Name the blood parasite species.
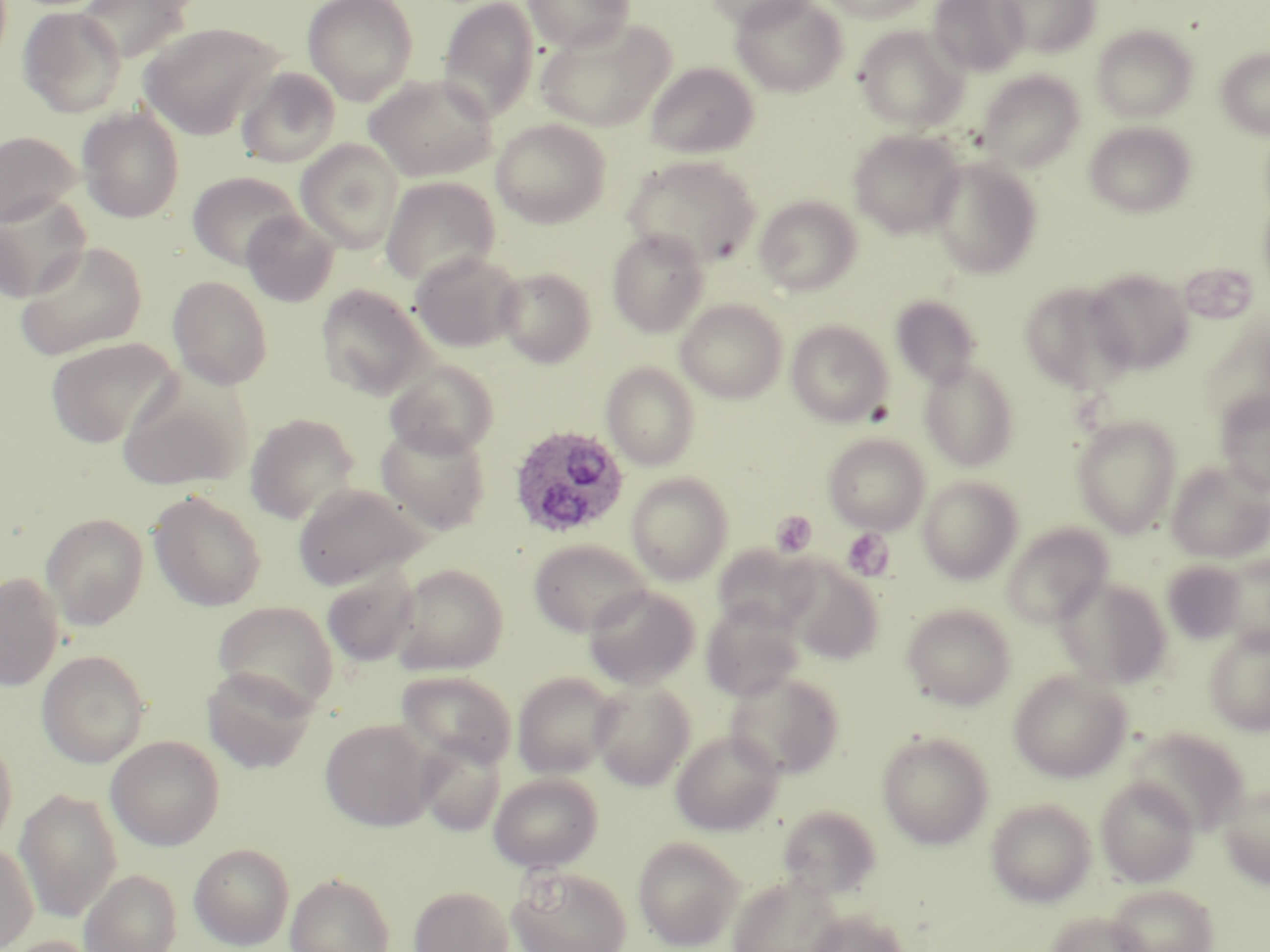

Plasmodium ovale.

magnification = 1000x
Plasmodium ovale-infected red blood cell locations = approximate bounding boxes as [x1, y1, x2, y2] in pixels: [508, 424, 629, 539]
field of view = one of a larger specimen
modality = light microscopy
image size = 1270×952 pixels
stain = May-Grünwald-Giemsa
uninfected red blood cell locations = approximate bounding boxes as [x1, y1, x2, y2] in pixels: [302, 0, 418, 104], [524, 0, 635, 52], [705, 0, 819, 30], [731, 0, 848, 97], [820, 0, 929, 23], [928, 0, 1029, 76], [997, 0, 1101, 58], [79, 1, 196, 62], [437, 1, 540, 121], [18, 6, 127, 118], [536, 17, 676, 131], [138, 22, 284, 138], [854, 25, 970, 132], [1091, 25, 1198, 123], [1216, 47, 1270, 138], [645, 62, 759, 158], [235, 66, 341, 168], [975, 70, 1085, 171], [364, 74, 497, 181], [77, 107, 185, 223], [491, 119, 611, 227], [1084, 121, 1196, 218], [848, 128, 966, 238], [0, 130, 83, 227], [296, 139, 404, 252], [622, 154, 761, 268], [929, 157, 1043, 279], [188, 171, 303, 270], [380, 176, 499, 286], [1, 195, 90, 302], [754, 195, 862, 296], [242, 211, 339, 307], [607, 228, 710, 337], [16, 240, 148, 360], [410, 250, 524, 352], [496, 266, 596, 367], [1084, 267, 1194, 375], [167, 275, 273, 390], [1019, 282, 1136, 395], [316, 284, 434, 400], [890, 293, 983, 390], [676, 299, 787, 403], [786, 319, 892, 427], [44, 337, 180, 448], [918, 358, 1020, 471], [383, 359, 500, 459], [601, 361, 700, 469], [116, 371, 252, 492], [1214, 390, 1270, 495], [244, 412, 361, 524], [1072, 416, 1181, 537], [375, 423, 491, 534], [824, 433, 930, 534], [1166, 461, 1270, 564], [626, 472, 734, 584], [917, 475, 1023, 584], [292, 482, 429, 590], [148, 490, 266, 612], [41, 513, 148, 629], [1002, 523, 1113, 626], [529, 538, 651, 636], [712, 544, 819, 635], [1218, 555, 1270, 652], [1162, 559, 1251, 644], [784, 561, 884, 664], [390, 563, 508, 674], [322, 568, 420, 668], [0, 571, 64, 690], [1055, 576, 1171, 689], [583, 584, 700, 689], [212, 601, 339, 715], [700, 602, 804, 701], [901, 603, 1016, 710], [1203, 628, 1270, 734], [37, 650, 150, 767], [202, 667, 316, 774], [1009, 669, 1132, 782], [397, 670, 516, 770], [725, 670, 845, 780], [512, 672, 621, 779], [591, 680, 696, 789], [320, 718, 437, 831], [1126, 727, 1251, 834], [671, 729, 784, 836], [876, 730, 995, 849], [0, 732, 18, 853], [106, 735, 224, 850], [415, 737, 506, 836], [489, 772, 602, 871], [1096, 776, 1199, 888], [1217, 781, 1270, 888], [15, 788, 123, 922], [986, 797, 1097, 907], [776, 804, 882, 899], [633, 836, 744, 950], [0, 840, 38, 952], [189, 843, 295, 950], [508, 866, 632, 952], [79, 868, 181, 952], [285, 872, 395, 952], [727, 874, 844, 952], [1105, 883, 1219, 952], [409, 885, 514, 952], [803, 908, 911, 952], [1045, 911, 1152, 952], [4, 935, 101, 952]
preparation = thin blood film
platelet locations = approximate bounding boxes as [x1, y1, x2, y2] in pixels: [770, 511, 817, 558], [841, 528, 893, 581]